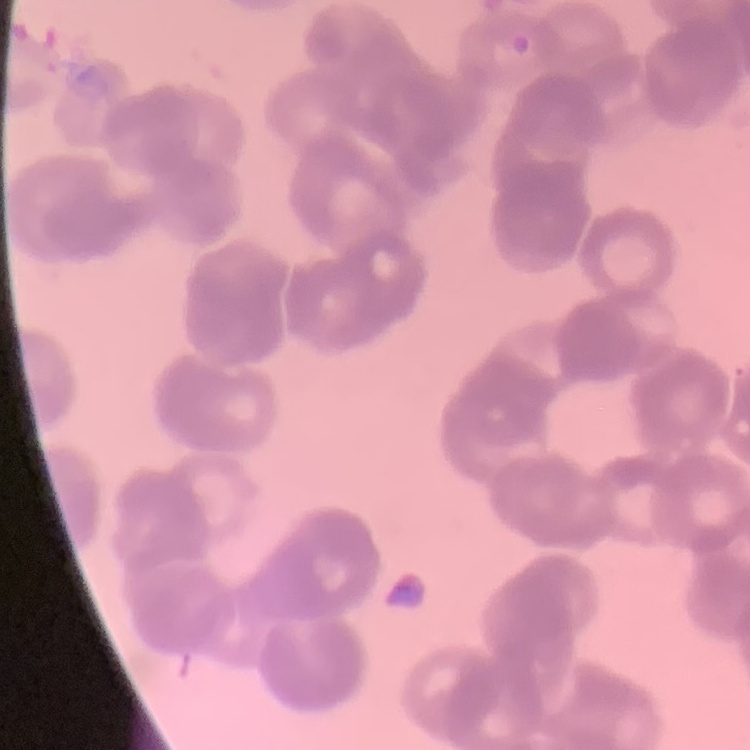

The erythrocytes exhibit rouleaux formation. Thin peripheral smear. One tile cut from a larger photomicrograph. Field's or Giemsa stain.